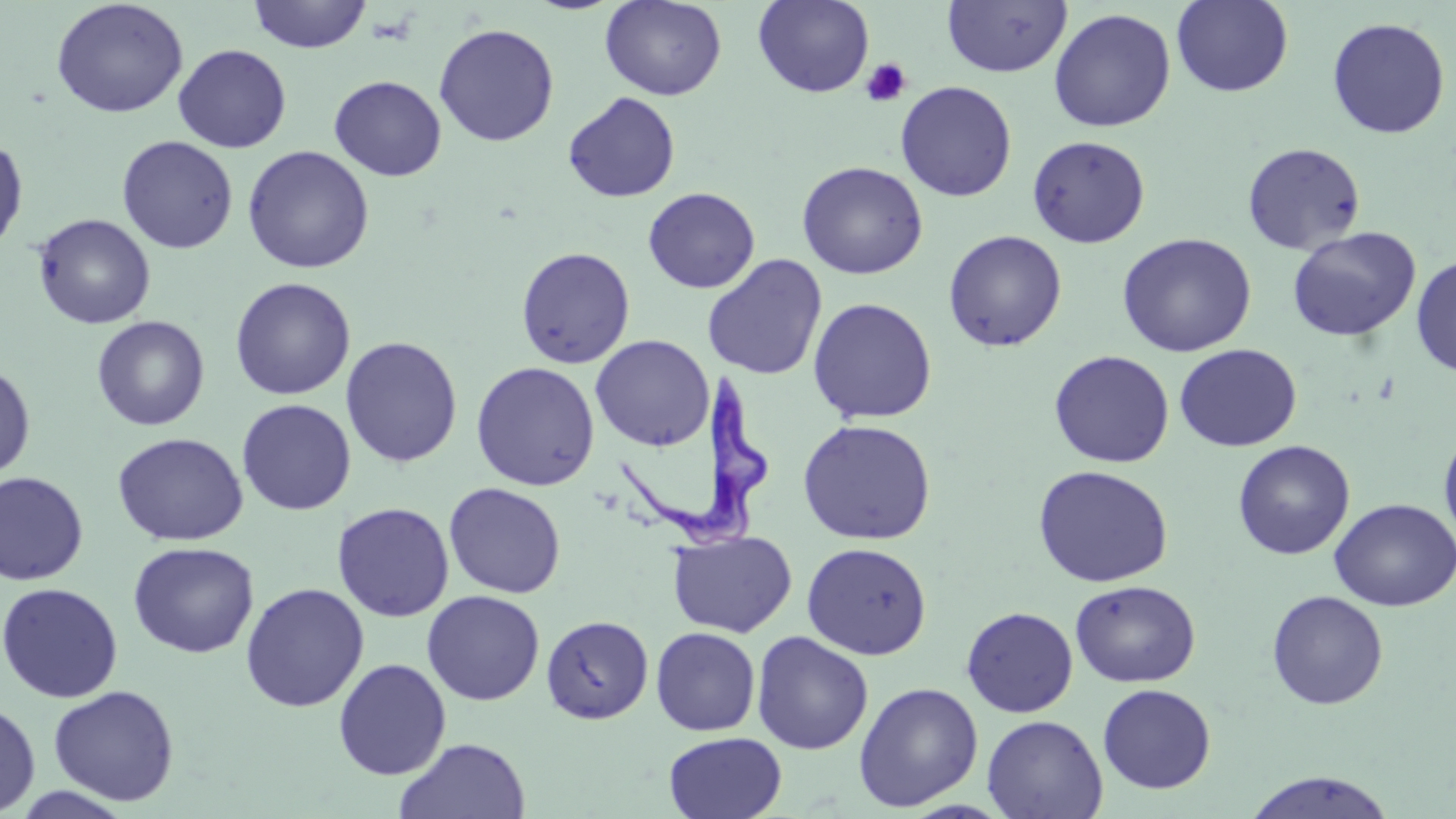

Approximate bounding boxes as (x1,y1)-(x2,y2) corner pairs in pixels. Trypanosoma brucei locations: (615,375)-(770,556). Platelet locations: (860,58)-(912,108). Uninfected red blood cell locations: (51,0)-(188,118), (247,0)-(371,53), (599,0)-(727,101), (753,1)-(874,97), (942,1)-(1072,78), (1171,1)-(1294,97), (1048,8)-(1176,132), (1326,16)-(1451,140), (433,23)-(559,146), (173,44)-(291,153), (328,75)-(447,181), (895,80)-(1017,202), (563,91)-(681,203), (0,135)-(28,254), (116,135)-(238,254), (1027,135)-(1151,248), (1242,142)-(1366,255), (242,145)-(375,274), (797,160)-(928,279), (643,187)-(760,293), (33,213)-(156,329), (1287,226)-(1421,342), (943,230)-(1067,352), (1116,232)-(1256,357), (516,246)-(636,369), (702,254)-(828,380), (1411,255)-(1456,377), (229,277)-(356,400), (807,297)-(938,423), (92,315)-(209,431), (590,334)-(714,451), (340,336)-(463,468), (1174,343)-(1302,451), (1048,350)-(1175,468), (471,361)-(600,491), (0,363)-(36,480), (236,399)-(356,515), (797,418)-(937,545), (1439,427)-(1456,550), (112,432)-(249,545), (1232,440)-(1355,559), (1033,464)-(1174,587), (0,471)-(89,585), (443,482)-(566,598), (1329,498)-(1456,611), (332,501)-(455,622), (668,531)-(797,638), (127,541)-(259,659), (802,542)-(932,659), (1070,579)-(1200,687), (0,582)-(123,703), (240,582)-(369,713), (422,590)-(545,705), (1266,590)-(1388,709), (961,606)-(1078,718), (540,614)-(654,724), (650,626)-(761,736), (751,631)-(873,754), (333,658)-(451,780), (853,682)-(983,811), (1097,683)-(1216,794), (48,684)-(180,806), (0,699)-(40,817), (982,714)-(1107,818), (663,731)-(787,819), (395,737)-(531,819), (1243,770)-(1398,819). Slide-level diagnosis: Trypanosoma brucei. Captured at 1000x magnification. Optical microscopy. Thin blood smear. May-Grünwald-Giemsa stain. Image is 1456×819 pixels. One field of a larger specimen.